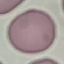
Result: no malaria parasites seen. Automatically extracted cell patch, resized to 64 × 64 pixels. Giemsa stain. Thin blood smear. Photographed with a smartphone camera at the microscope eyepiece.